Report the malaria status of this cell.
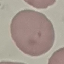
Uninfected.

Thin smear of blood. Automatically extracted cell patch, resized to 64 × 64 pixels. Photographed with a smartphone camera at the microscope eyepiece. Giemsa-stained preparation.